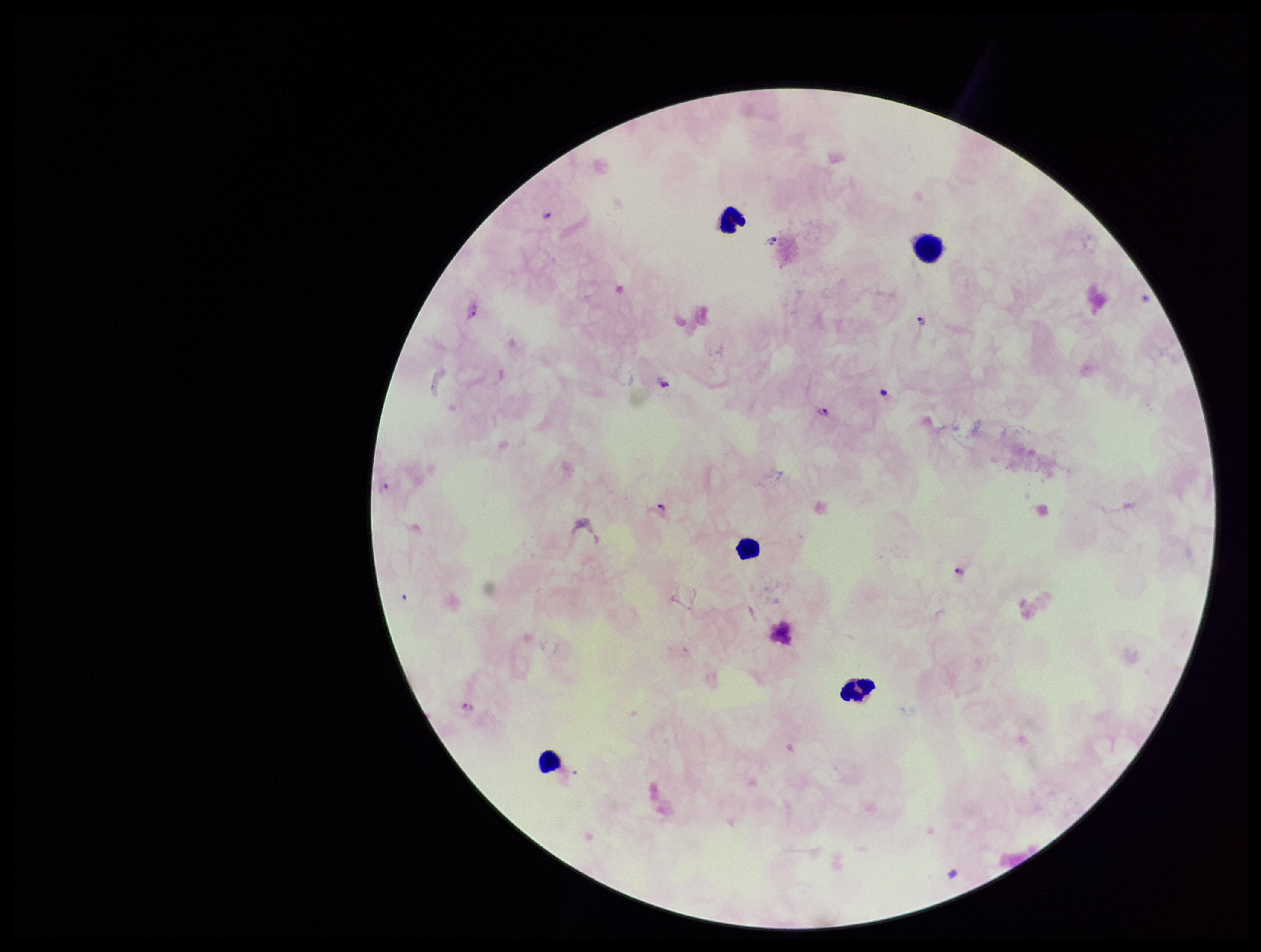

Leukocyte count: 5. Single field of view. Image is 1261×952 pixels. Plasmodium parasites: identified. Preparation: thick smear. Smartphone photograph taken through the eyepiece of a microscope. Parasite count: 11. Stained with Giemsa. Species reported for this patient: Plasmodium falciparum. Patient malaria status: positive.